Name the cell type shown.
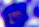

A leukocyte.

modality = micrograph
magnification = 400x